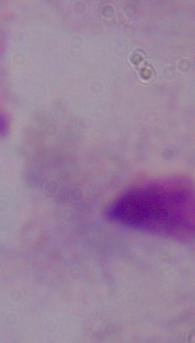
Summary:
  - Identification: trichomonad
  - Magnification: 1000x
  - Modality: micrograph